Report the malaria status of this cell.
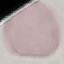
Uninfected.

Acquired by smartphone through the microscope eyepiece. Thin blood film. Giemsa-stained preparation. Automatically extracted cell patch, resized to 64 × 64 pixels.